Locate every leukocyte (white blood cell).
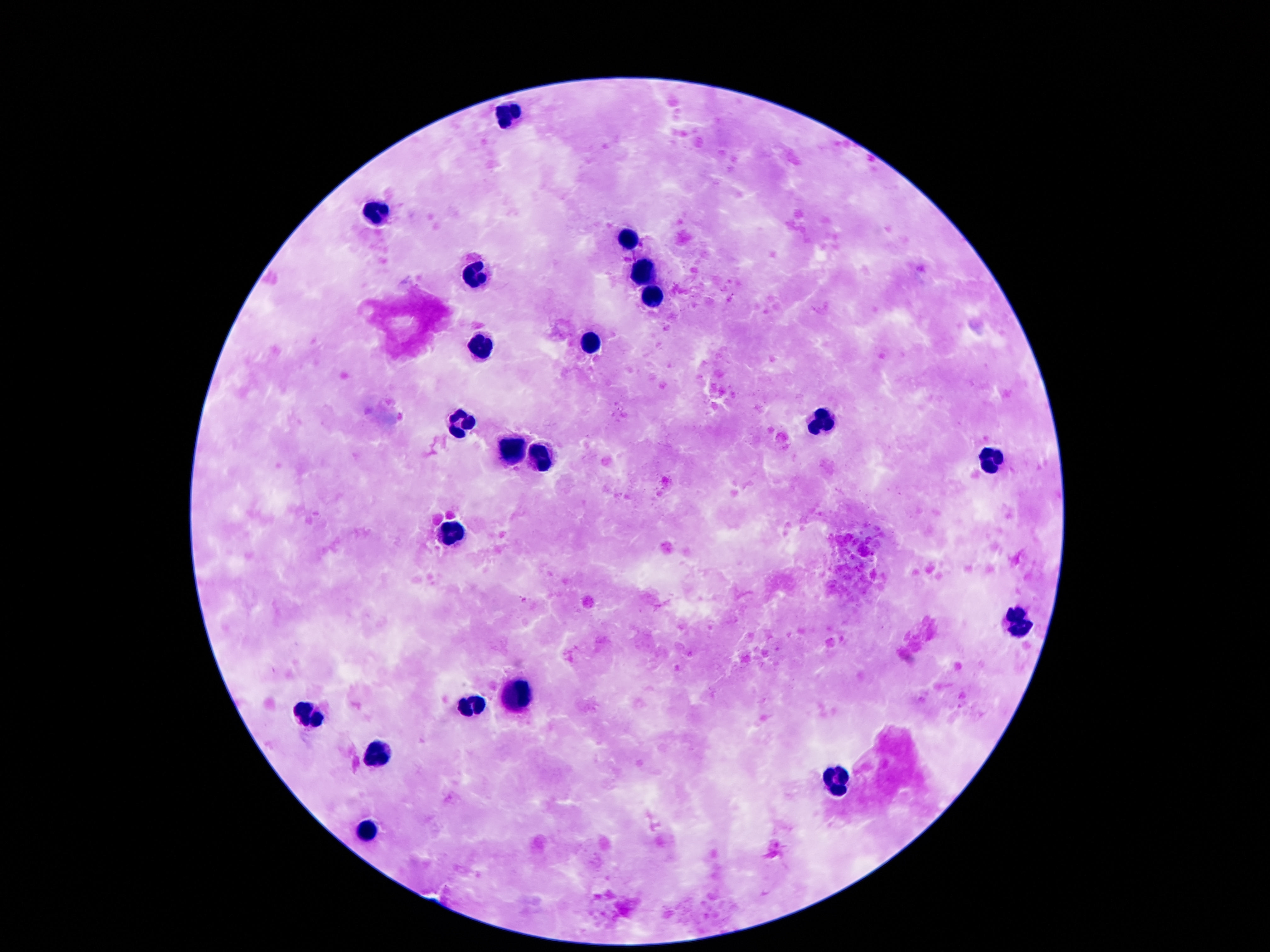
Approximate centers as {x, y} in pixels.
Leukocytes: {504, 113}, {376, 213}, {625, 235}, {640, 273}, {476, 279}, {651, 298}, {594, 342}, {483, 346}, {819, 422}, {460, 426}, {510, 451}, {987, 459}, {533, 461}, {449, 533}, {1018, 624}, {518, 695}, {470, 708}, {308, 716}, {374, 752}, {840, 781}, {367, 834}.

Thick peripheral-blood smear. Image is 1270×952 pixels. 100x magnification. Patient malaria status: negative. Giemsa stain. Photographed through the microscope eyepiece with a smartphone camera. One field from this slide.